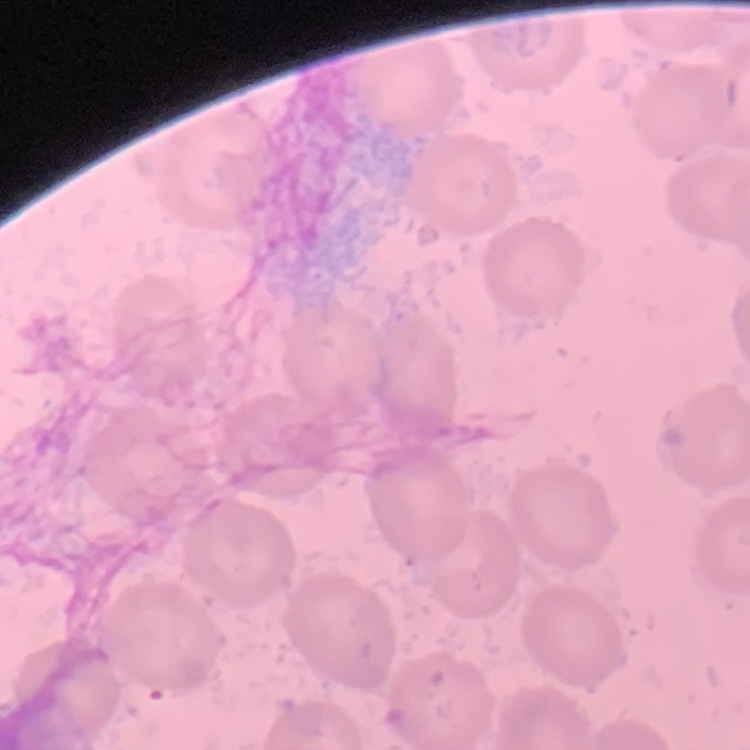 The red blood cells show no rouleaux formation. One tile cut from a larger photomicrograph. Thin blood film. Field's or Giemsa stain.